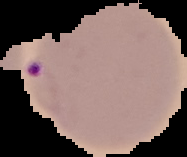
Summary:
  - Preparation: thin blood smear
  - Image size: 187×157 pixels
  - Image type: segmented cell region on a black background
  - Result: malaria parasites detected